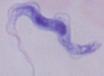
Summary:
  - Magnification: 1000x
  - Modality: micrograph
  - Identification: trypanosome